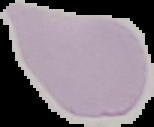

Summary:
  - Image type: segmented cell region with the area outside set to black
  - Image size: 154×127 pixels
  - Result: no malaria parasites detected
  - Preparation: thin blood film